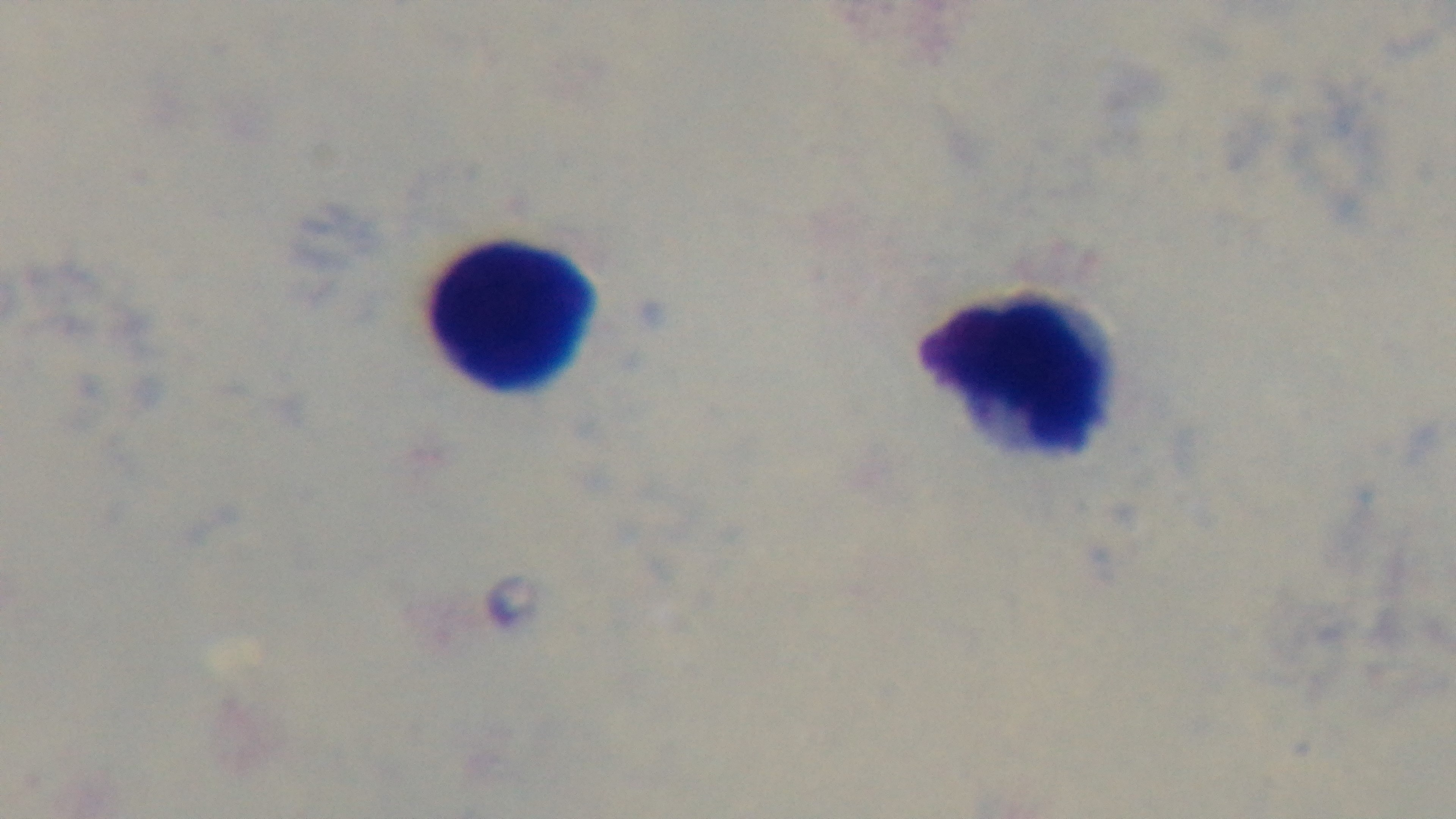 One field from the slide. Photomicrograph. Malaria status: uninfected. Oil-immersion objective, 100x. Preparation: thick blood film. Mounted 4K digital camera. Giemsa-stained.